Classify this cell by malaria status.
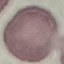

Uninfected.

{
  "capture": "smartphone through the microscope eyepiece",
  "preparation": "thin blood smear",
  "stain": "Giemsa",
  "image_type": "automatically extracted cell patch, resized to 64 × 64 pixels"
}